Classify this cell by malaria status.
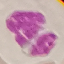

Uninfected.

Summary:
  - Stain: Giemsa
  - Preparation: thin blood smear
  - Image type: automatically extracted cell patch, resized to 64 × 64 pixels
  - Capture: smartphone camera at the microscope eyepiece